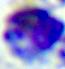

Summary:
  - Modality: photomicrograph
  - Identification: leukocyte
  - Magnification: 400x